Look for Plasmodium parasites.
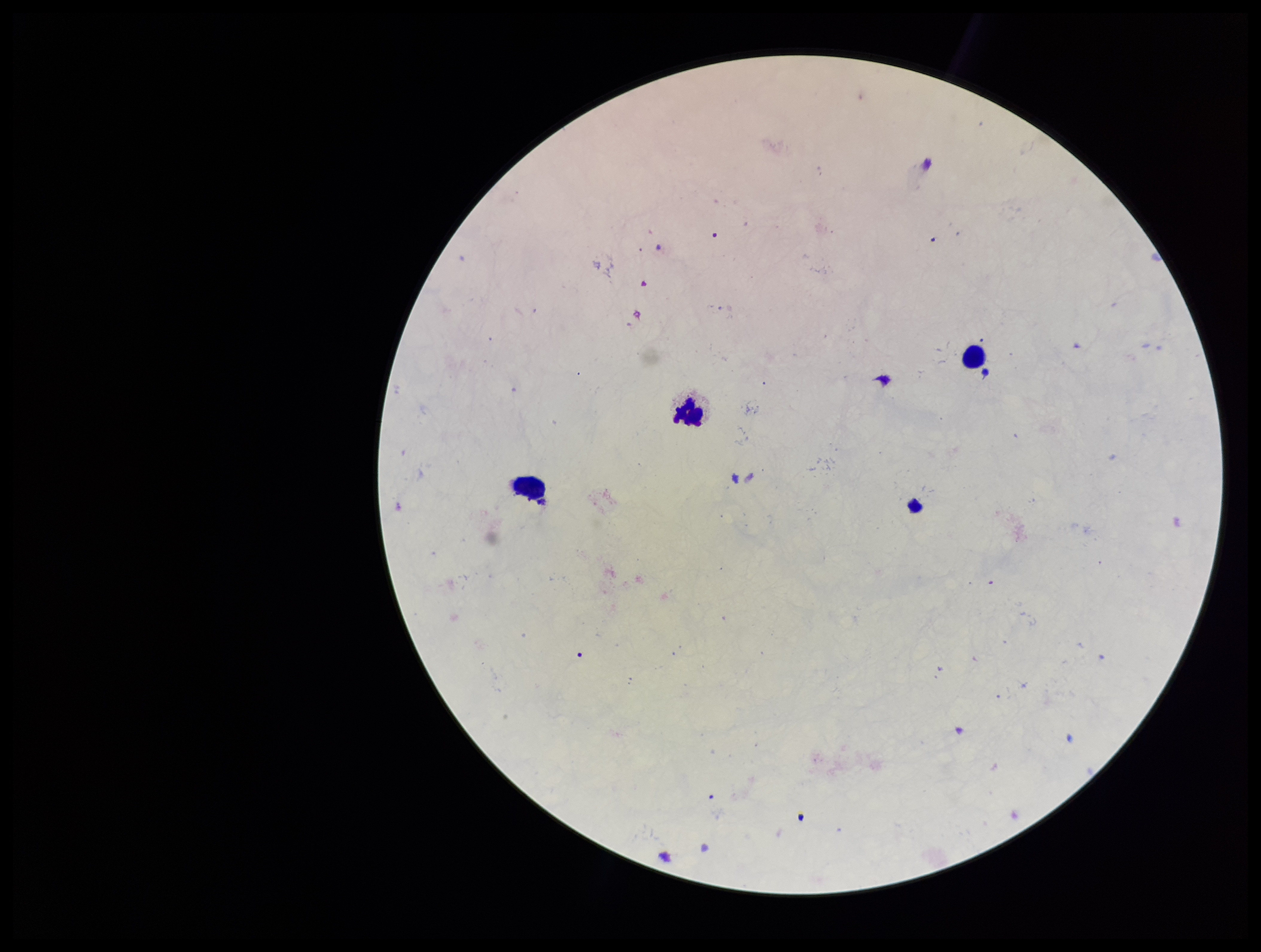

None detected.

Summary:
  - Capture: smartphone photograph through the microscope eyepiece
  - Leukocyte count: 3
  - Field of view: one from this slide
  - Image size: 1261×952 pixels
  - Parasite count: 0
  - Preparation: thick smear
  - Stain: Giemsa
  - Patient malaria status: negative